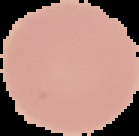 Image is 139×136 pixels. Result: negative for Plasmodium parasites. From a thin blood film. Segmented cell region on a black background.